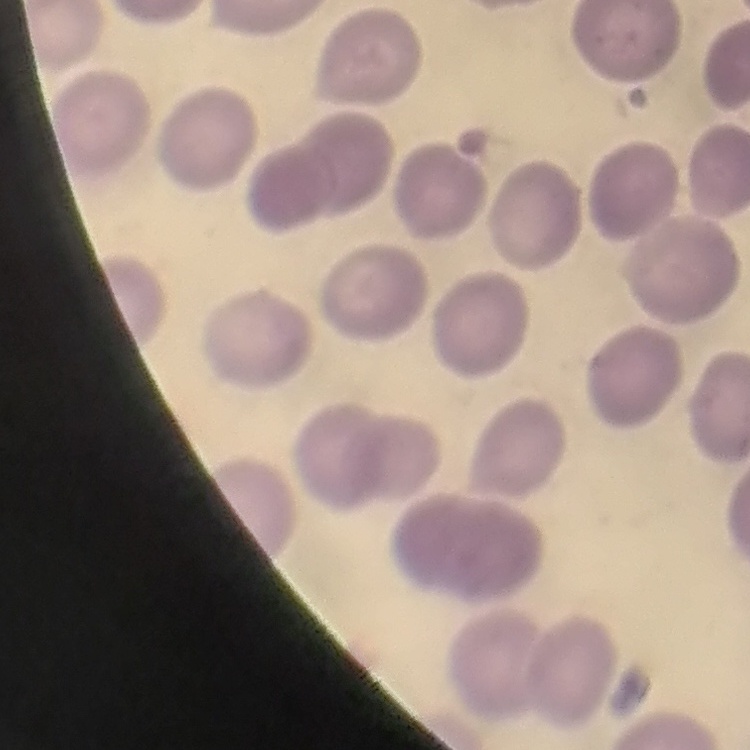

The erythrocytes exhibit no rouleaux formation. Field's or Giemsa stain. Thin blood film. Square crop of a larger photomicrograph.